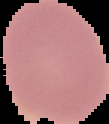

Summary:
  - Preparation: thin blood film
  - Malaria status: uninfected
  - Image type: segmented cell region on a black background
  - Image size: 109×124 pixels